Identify the parasite.
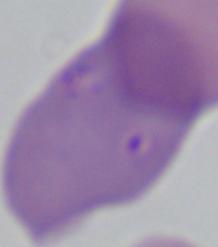

Babesia.

Captured at 1000x magnification. Photomicrograph.